Name the blood parasite species.
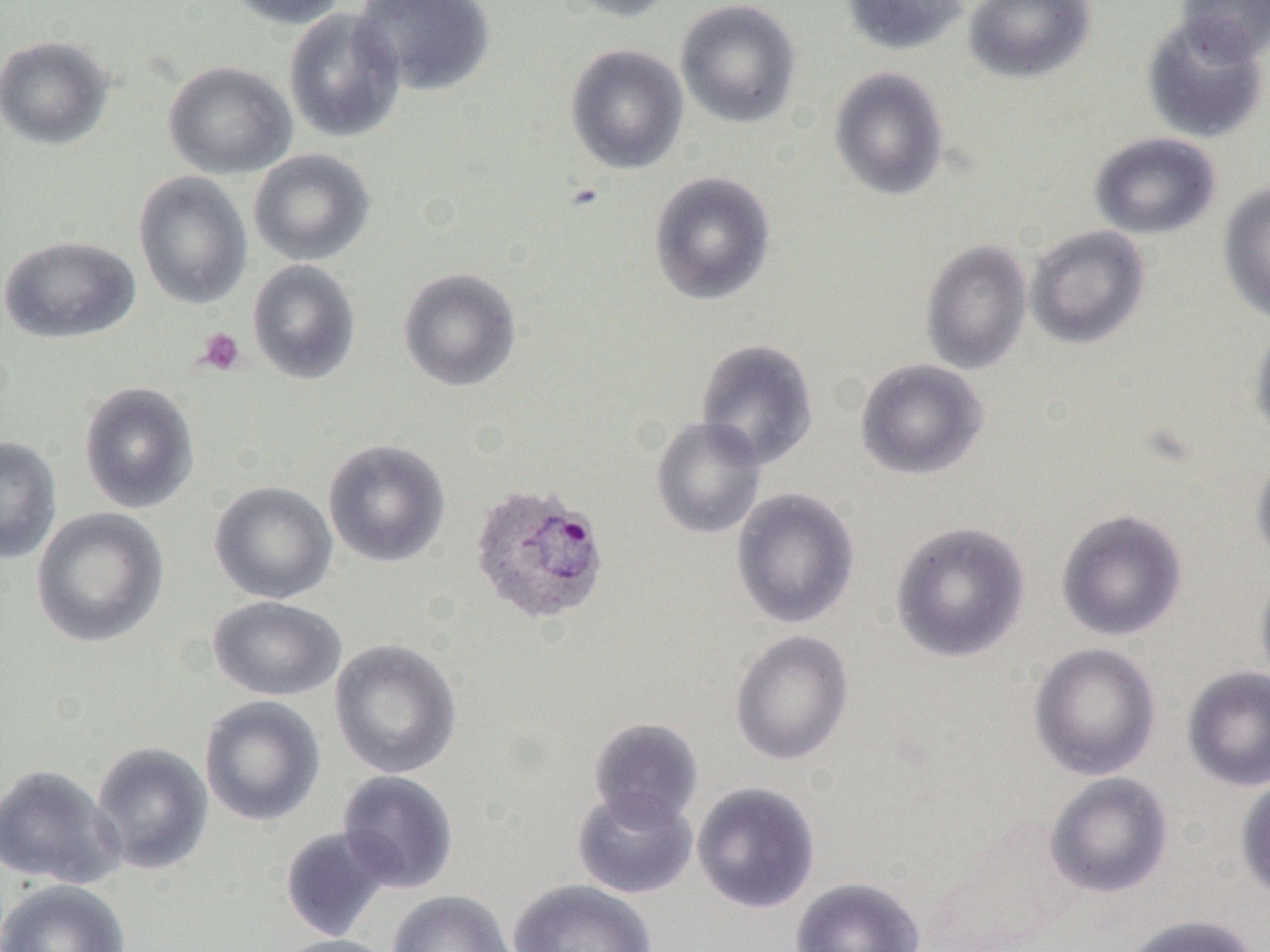
Plasmodium ovale.

Summary:
  - Coordinate format: approximate bounding boxes as (x1,y1)-(x2,y2) corner pairs in pixels
  - Platelet locations: (196,328)-(246,375)
  - Plasmodium ovale-infected red blood cell locations: (469,483)-(611,626)
  - Uninfected red blood cell locations: (223,0)-(349,29), (352,0)-(496,97), (553,0)-(679,23), (675,0)-(801,129), (841,0)-(969,55), (964,0)-(1095,83), (1175,1)-(1270,63), (283,7)-(406,144), (1141,16)-(1268,144), (0,35)-(114,150), (565,44)-(689,174), (163,60)-(297,179), (828,67)-(949,200), (1089,132)-(1221,240), (249,149)-(375,266), (648,170)-(776,306), (133,171)-(252,310), (1218,183)-(1270,324), (1025,225)-(1151,349), (0,235)-(140,345), (920,239)-(1033,375), (247,259)-(361,384), (398,267)-(522,392), (1249,322)-(1270,447), (694,338)-(820,470), (855,358)-(988,480), (78,381)-(200,514), (650,416)-(767,539), (0,435)-(62,565), (323,439)-(450,568), (1250,454)-(1270,566), (209,481)-(338,604), (731,487)-(861,629), (30,507)-(169,648), (1056,509)-(1188,641), (889,520)-(1030,663), (1255,565)-(1270,693), (207,596)-(346,701), (729,630)-(854,766), (329,638)-(462,779), (1029,642)-(1161,780), (1182,666)-(1270,791), (199,695)-(326,827), (588,717)-(704,828), (91,741)-(213,875), (0,764)-(124,889), (336,770)-(460,894), (1044,772)-(1173,898), (1235,775)-(1270,904), (691,781)-(821,914), (571,787)-(698,898), (278,826)-(393,942), (790,876)-(926,952), (0,879)-(131,952), (508,879)-(657,952), (387,890)-(515,952), (1119,914)-(1260,952), (272,934)-(400,952)
  - Preparation: thin blood smear
  - Image size: 1270×952 pixels
  - Field of view: one of a larger specimen
  - Modality: light microscopy
  - Magnification: 1000x